Identify the cell.
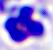
A leukocyte.

Summary:
  - Modality: micrograph
  - Magnification: 400x